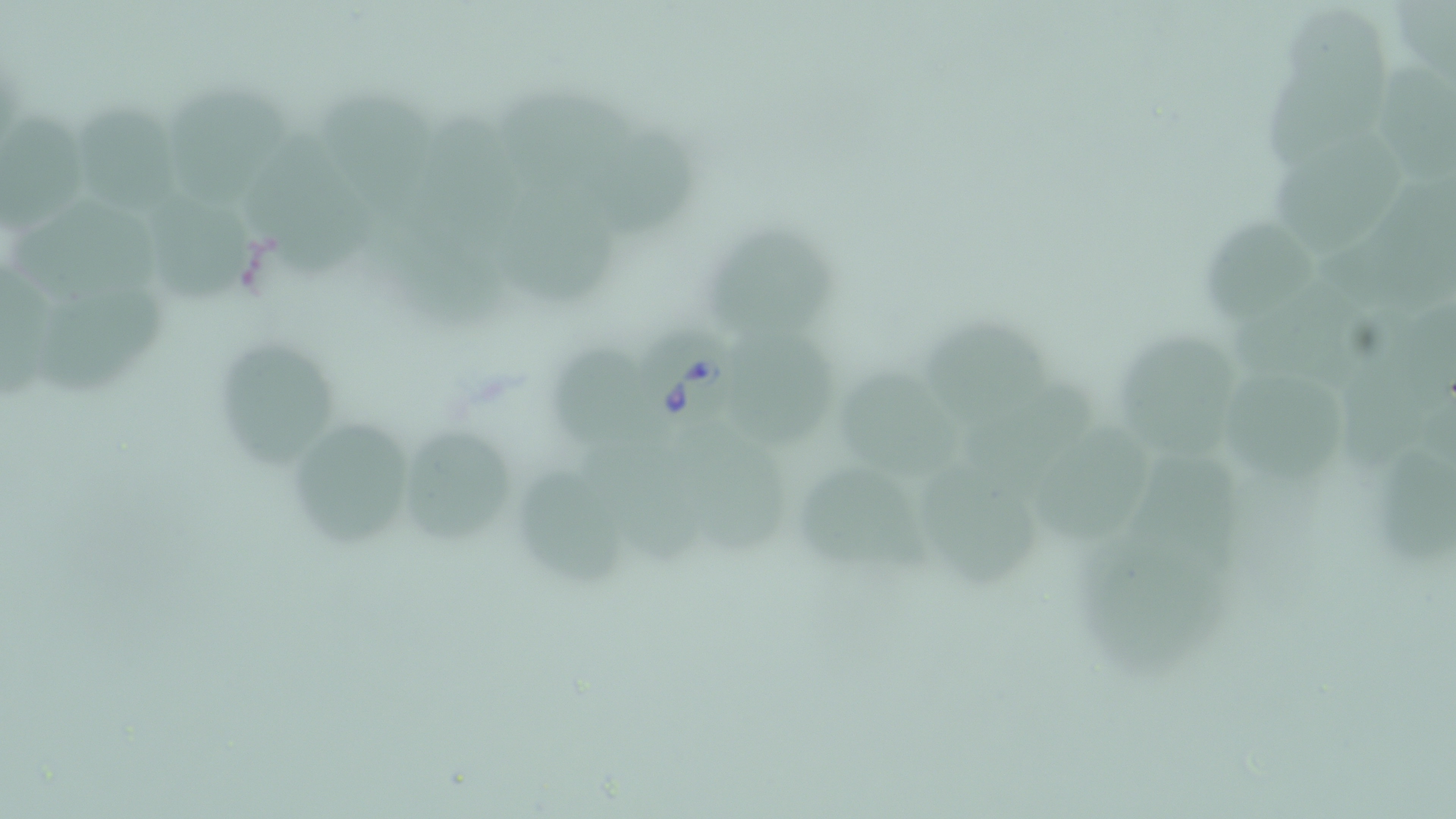
Babesia divergens-infected red blood cell locations = approximate bounding boxes as (x1, y1, x2, y2) in pixels: (631, 318, 740, 443)
slide-level diagnosis = Babesia divergens
preparation = thin blood smear
stain = May-Grünwald-Giemsa
modality = light microscopy
image size = 1456×819 pixels
magnification = 1000x
uninfected red blood cell locations = approximate bounding boxes as (x1, y1, x2, y2) in pixels: (1284, 7, 1391, 107), (1367, 55, 1456, 188), (1263, 70, 1394, 176), (495, 84, 646, 196), (166, 86, 283, 205), (315, 91, 436, 206), (73, 101, 186, 215), (2, 111, 87, 226), (402, 111, 538, 242), (591, 127, 707, 242), (242, 128, 386, 288), (1271, 135, 1406, 262), (139, 185, 265, 305), (508, 186, 622, 311), (1322, 187, 1456, 312), (9, 195, 164, 310), (1191, 217, 1317, 331), (705, 221, 837, 352), (382, 223, 518, 336), (1230, 273, 1393, 385), (38, 289, 164, 398), (1387, 299, 1454, 410), (924, 318, 1056, 428), (727, 322, 839, 450), (1111, 328, 1246, 464), (210, 335, 346, 468), (551, 339, 660, 460), (1336, 356, 1428, 480), (1226, 363, 1348, 489), (839, 367, 964, 483), (966, 375, 1097, 477), (286, 415, 421, 552), (394, 420, 531, 552), (1035, 420, 1157, 548), (681, 426, 797, 562), (1380, 440, 1456, 570), (588, 441, 718, 564), (1121, 451, 1250, 578), (794, 459, 940, 582), (924, 461, 1039, 590), (515, 465, 637, 592), (1079, 525, 1243, 682)
field of view = single